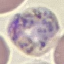
Summary:
  - Malaria status: parasitized
  - Image type: cell patch, automatically extracted from a larger field of view and resized to 64 × 64 pixels
  - Stain: Giemsa
  - Capture: smartphone camera at the microscope eyepiece
  - Preparation: thin blood smear